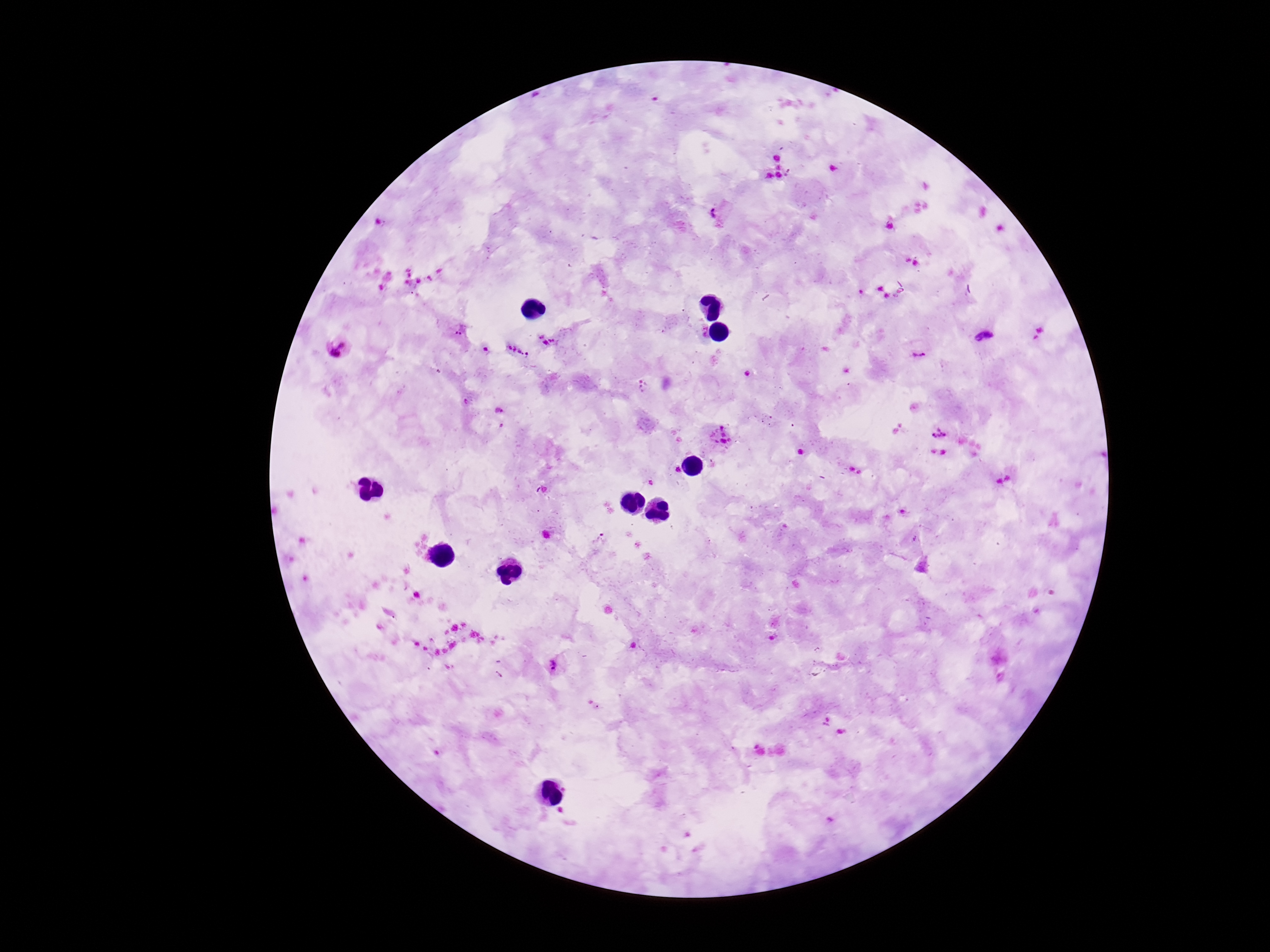
Approximate centers as [x, y] in pixels.
Summary:
  - Plasmodium parasite locations: [718, 215], [889, 226], [907, 259], [917, 263], [879, 286], [862, 292], [888, 298], [460, 331], [987, 335], [547, 340], [341, 347], [517, 351], [919, 356], [643, 388], [500, 409], [941, 430], [721, 434], [601, 539], [554, 666]
  - Preparation: thick peripheral-blood smear
  - Image size: 1270×952 pixels
  - Stain: Giemsa
  - Magnification: 100x
  - Capture: smartphone camera through the microscope eyepiece
  - Field of view: single
  - Patient malaria status: infected